Assess for Plasmodium parasites.
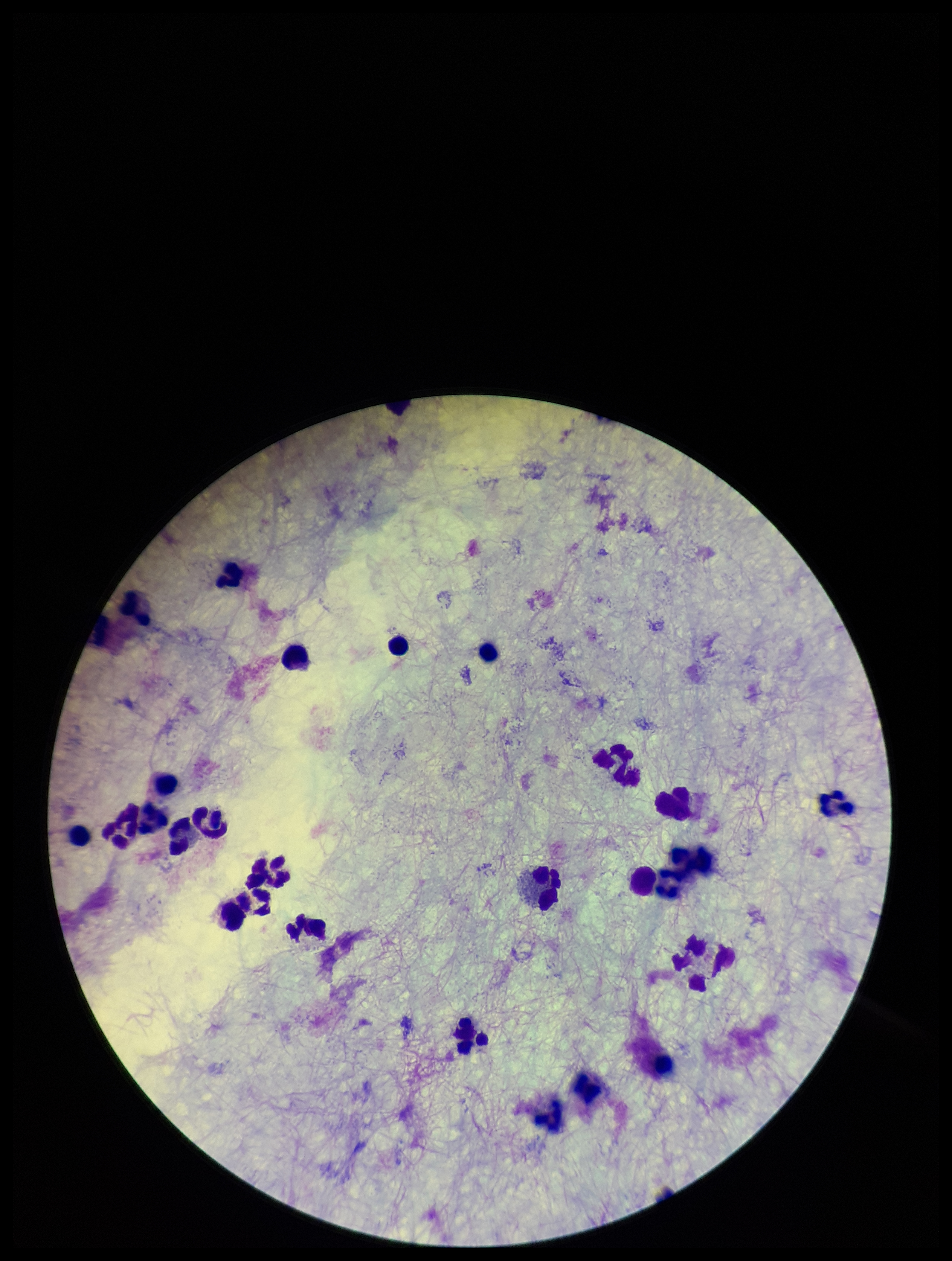
None seen.

Stained with Giemsa. One field from this slide. Preparation: thick smear. Image is 952×1261 pixels. Patient malaria status: negative. Parasite count: 0. Photographed through the microscope eyepiece with a smartphone camera. Leukocyte count: 22.